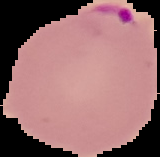
Summary:
  - Image size: 160×157 pixels
  - Malaria status: parasitized
  - Preparation: thin blood smear
  - Image type: segmented cell region on a black background